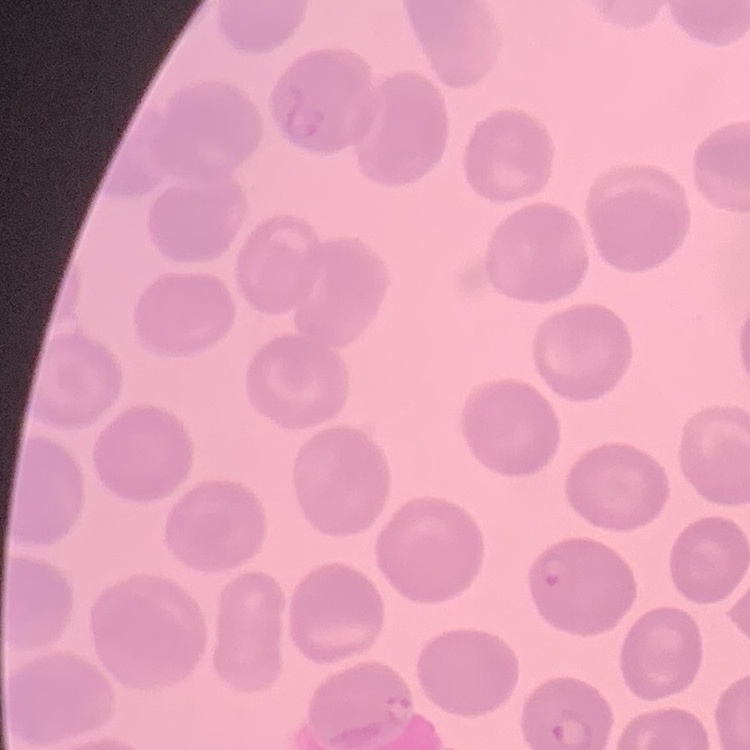

The erythrocytes show no rouleaux formation. Thin blood film. Stained with either Field's or Giemsa. Square crop of a larger photomicrograph.